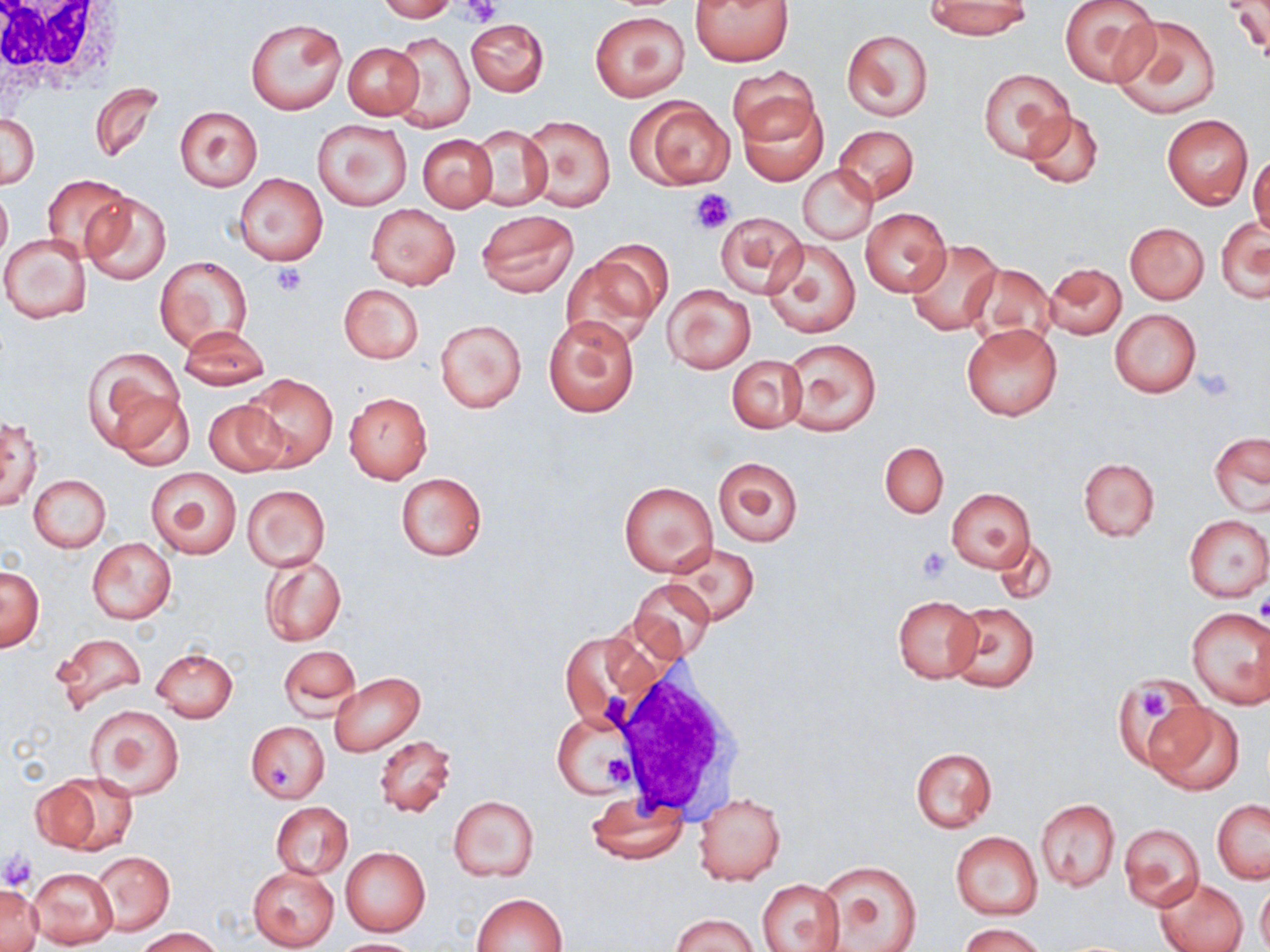
slide-level diagnosis = no evidence of blood parasites
stain = May-Grünwald-Giemsa
field of view = one of a larger specimen
uninfected red blood cell locations = approximate bounding boxes as named x1/y1/x2/y2 corners in pixels: (x1=376, y1=0, x2=457, y2=22), (x1=690, y1=0, x2=794, y2=66), (x1=926, y1=0, x2=1031, y2=38), (x1=1058, y1=0, x2=1160, y2=88), (x1=1223, y1=1, x2=1269, y2=58), (x1=591, y1=11, x2=688, y2=100), (x1=245, y1=15, x2=347, y2=115), (x1=1111, y1=15, x2=1221, y2=120), (x1=465, y1=17, x2=549, y2=96), (x1=841, y1=29, x2=933, y2=120), (x1=390, y1=33, x2=475, y2=132), (x1=343, y1=43, x2=422, y2=120), (x1=728, y1=65, x2=818, y2=145), (x1=978, y1=68, x2=1073, y2=161), (x1=89, y1=83, x2=163, y2=163), (x1=734, y1=93, x2=830, y2=184), (x1=629, y1=96, x2=734, y2=190), (x1=175, y1=106, x2=262, y2=191), (x1=1021, y1=109, x2=1104, y2=188), (x1=2, y1=114, x2=39, y2=188), (x1=1162, y1=114, x2=1252, y2=209), (x1=524, y1=116, x2=616, y2=212), (x1=313, y1=118, x2=410, y2=211), (x1=468, y1=125, x2=553, y2=212), (x1=834, y1=125, x2=918, y2=202), (x1=418, y1=134, x2=498, y2=212), (x1=1249, y1=153, x2=1270, y2=243), (x1=799, y1=164, x2=877, y2=245), (x1=233, y1=172, x2=328, y2=265), (x1=41, y1=174, x2=134, y2=263), (x1=0, y1=182, x2=12, y2=266), (x1=82, y1=192, x2=172, y2=286), (x1=366, y1=204, x2=460, y2=289), (x1=861, y1=208, x2=952, y2=296), (x1=476, y1=210, x2=578, y2=296), (x1=715, y1=212, x2=807, y2=297), (x1=1216, y1=216, x2=1270, y2=303), (x1=1124, y1=223, x2=1209, y2=303), (x1=1, y1=233, x2=91, y2=324), (x1=763, y1=236, x2=861, y2=338), (x1=907, y1=240, x2=1001, y2=335), (x1=569, y1=244, x2=668, y2=345), (x1=156, y1=256, x2=252, y2=353), (x1=1045, y1=262, x2=1126, y2=340), (x1=962, y1=263, x2=1057, y2=349), (x1=339, y1=284, x2=424, y2=364), (x1=662, y1=284, x2=756, y2=372), (x1=1110, y1=308, x2=1201, y2=398), (x1=543, y1=316, x2=640, y2=418), (x1=434, y1=318, x2=527, y2=413), (x1=962, y1=322, x2=1062, y2=421), (x1=178, y1=326, x2=269, y2=391), (x1=782, y1=338, x2=882, y2=436), (x1=84, y1=348, x2=187, y2=456), (x1=727, y1=354, x2=807, y2=433), (x1=241, y1=372, x2=338, y2=470), (x1=111, y1=391, x2=197, y2=472), (x1=344, y1=391, x2=431, y2=484), (x1=202, y1=399, x2=288, y2=476), (x1=0, y1=412, x2=43, y2=511), (x1=1210, y1=434, x2=1270, y2=516), (x1=880, y1=441, x2=949, y2=518), (x1=713, y1=457, x2=802, y2=546), (x1=1078, y1=457, x2=1159, y2=542), (x1=147, y1=467, x2=242, y2=560), (x1=396, y1=472, x2=487, y2=561), (x1=30, y1=474, x2=110, y2=552), (x1=620, y1=481, x2=717, y2=576), (x1=241, y1=485, x2=330, y2=571), (x1=946, y1=488, x2=1035, y2=572), (x1=1183, y1=514, x2=1269, y2=601), (x1=991, y1=535, x2=1057, y2=606), (x1=87, y1=538, x2=175, y2=625), (x1=670, y1=542, x2=759, y2=625), (x1=261, y1=556, x2=346, y2=646), (x1=1, y1=566, x2=44, y2=650), (x1=630, y1=580, x2=715, y2=661), (x1=892, y1=595, x2=984, y2=684), (x1=948, y1=601, x2=1040, y2=693), (x1=1185, y1=608, x2=1270, y2=708), (x1=559, y1=629, x2=652, y2=725), (x1=50, y1=630, x2=148, y2=716), (x1=279, y1=646, x2=359, y2=717), (x1=151, y1=648, x2=237, y2=722), (x1=330, y1=672, x2=423, y2=755), (x1=1117, y1=681, x2=1208, y2=770), (x1=1148, y1=702, x2=1242, y2=796), (x1=86, y1=704, x2=184, y2=799), (x1=552, y1=714, x2=637, y2=798), (x1=247, y1=722, x2=329, y2=802), (x1=374, y1=734, x2=455, y2=817), (x1=909, y1=747, x2=997, y2=832), (x1=30, y1=775, x2=135, y2=853), (x1=586, y1=793, x2=688, y2=864), (x1=693, y1=793, x2=786, y2=885), (x1=449, y1=796, x2=539, y2=882), (x1=1035, y1=799, x2=1121, y2=891), (x1=1212, y1=800, x2=1269, y2=883), (x1=271, y1=802, x2=353, y2=879), (x1=1119, y1=823, x2=1204, y2=911), (x1=950, y1=832, x2=1042, y2=920), (x1=341, y1=847, x2=429, y2=937), (x1=94, y1=851, x2=174, y2=934), (x1=815, y1=860, x2=921, y2=952), (x1=247, y1=865, x2=340, y2=951), (x1=28, y1=866, x2=117, y2=947), (x1=757, y1=878, x2=845, y2=952), (x1=1155, y1=878, x2=1248, y2=952), (x1=1257, y1=881, x2=1270, y2=952), (x1=1, y1=882, x2=41, y2=952), (x1=473, y1=892, x2=568, y2=952), (x1=672, y1=913, x2=757, y2=952), (x1=960, y1=922, x2=1045, y2=952), (x1=136, y1=927, x2=226, y2=952), (x1=333, y1=938, x2=419, y2=951)
white blood cell locations = approximate bounding boxes as named x1/y1/x2/y2 corners in pixels: (x1=0, y1=0, x2=129, y2=99), (x1=604, y1=661, x2=745, y2=819)
image size = 1270×952 pixels
modality = optical microscopy
platelet locations = approximate bounding boxes as named x1/y1/x2/y2 corners in pixels: (x1=462, y1=0, x2=500, y2=26), (x1=689, y1=188, x2=734, y2=234), (x1=271, y1=264, x2=307, y2=296), (x1=1198, y1=369, x2=1232, y2=402), (x1=916, y1=546, x2=953, y2=581), (x1=1255, y1=594, x2=1270, y2=626), (x1=1140, y1=688, x2=1174, y2=719), (x1=601, y1=753, x2=635, y2=791), (x1=267, y1=764, x2=291, y2=793), (x1=0, y1=848, x2=36, y2=892)
magnification = 1000x
preparation = thin blood smear